Name the parasite shown.
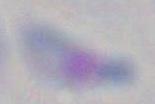
Toxoplasma gondii.

modality = micrograph
magnification = 1000x